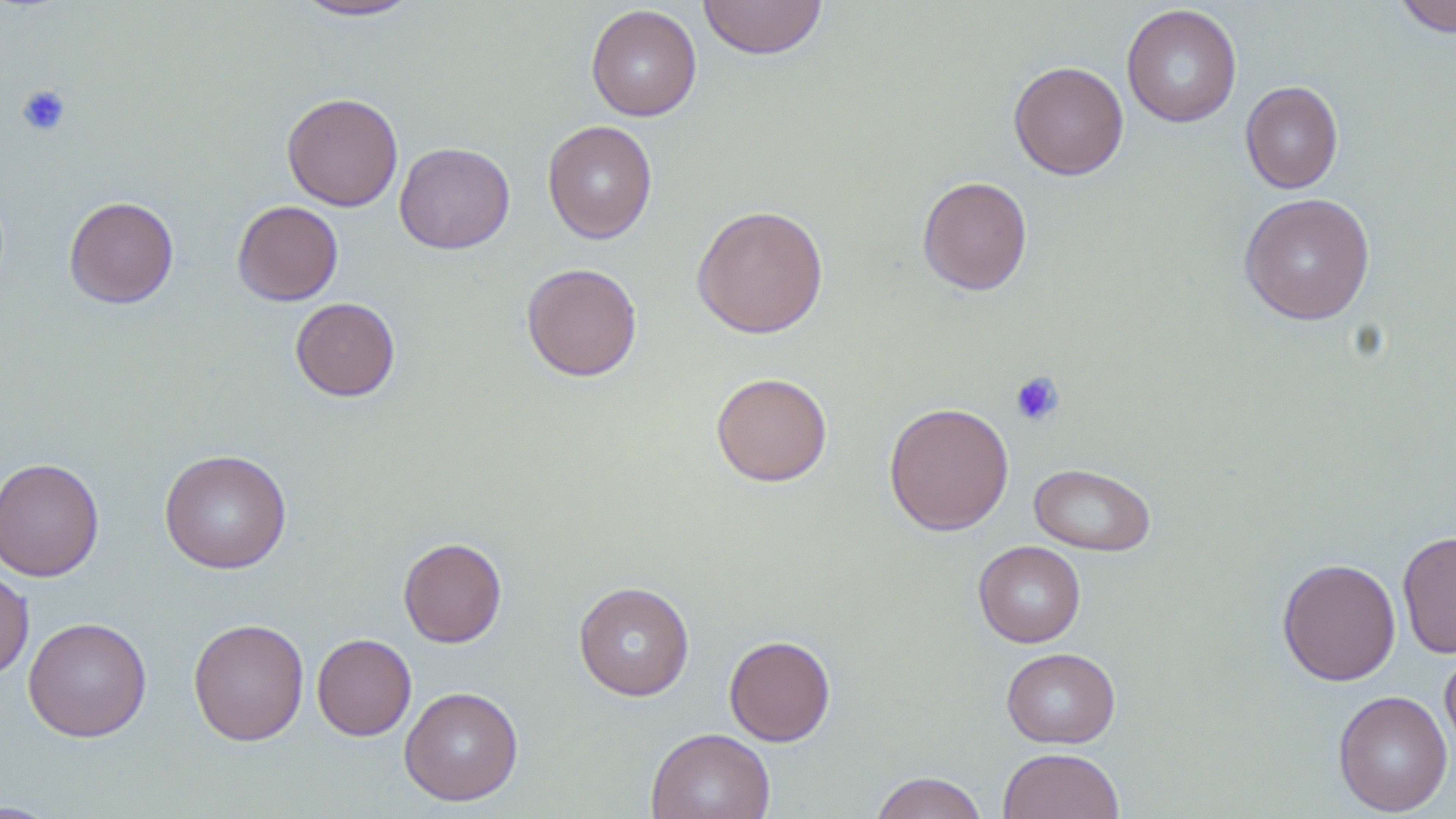

Approximate bounding boxes as [x1, y1, x2, y2] in pixels. Platelet locations: [16, 84, 71, 136], [1009, 371, 1064, 426]. Uninfected red blood cell locations: [698, 0, 828, 59], [1392, 0, 1456, 37], [291, 1, 422, 21], [585, 4, 702, 121], [1122, 4, 1242, 128], [1009, 61, 1129, 180], [1241, 81, 1344, 193], [281, 92, 403, 211], [542, 120, 658, 243], [394, 141, 515, 254], [917, 176, 1033, 295], [1239, 192, 1376, 325], [64, 196, 179, 309], [232, 200, 343, 306], [691, 205, 829, 338], [521, 262, 642, 381], [290, 297, 400, 401], [710, 371, 833, 486], [883, 402, 1014, 535], [159, 448, 292, 574], [0, 457, 105, 582], [1029, 463, 1155, 556], [1397, 530, 1456, 658], [398, 536, 507, 647], [973, 540, 1086, 647], [1277, 557, 1401, 685], [0, 566, 34, 682], [573, 581, 694, 700], [23, 616, 152, 742], [188, 617, 309, 746], [312, 633, 416, 740], [724, 635, 836, 746], [1001, 647, 1120, 748], [1440, 647, 1456, 759], [399, 686, 524, 806], [1333, 690, 1453, 816], [645, 728, 776, 819], [998, 747, 1125, 819], [870, 771, 988, 819], [0, 800, 64, 818]. Slide-level diagnosis: negative for blood parasites. May-Grünwald-Giemsa-stained preparation. Captured at 1000x magnification. Image is 1456×819 pixels. Light microscopy. Thin blood film. Single field of view.